Locate the cells, classifying each as a parasitized red blood cell, an uninfected red blood cell, or a white blood cell.
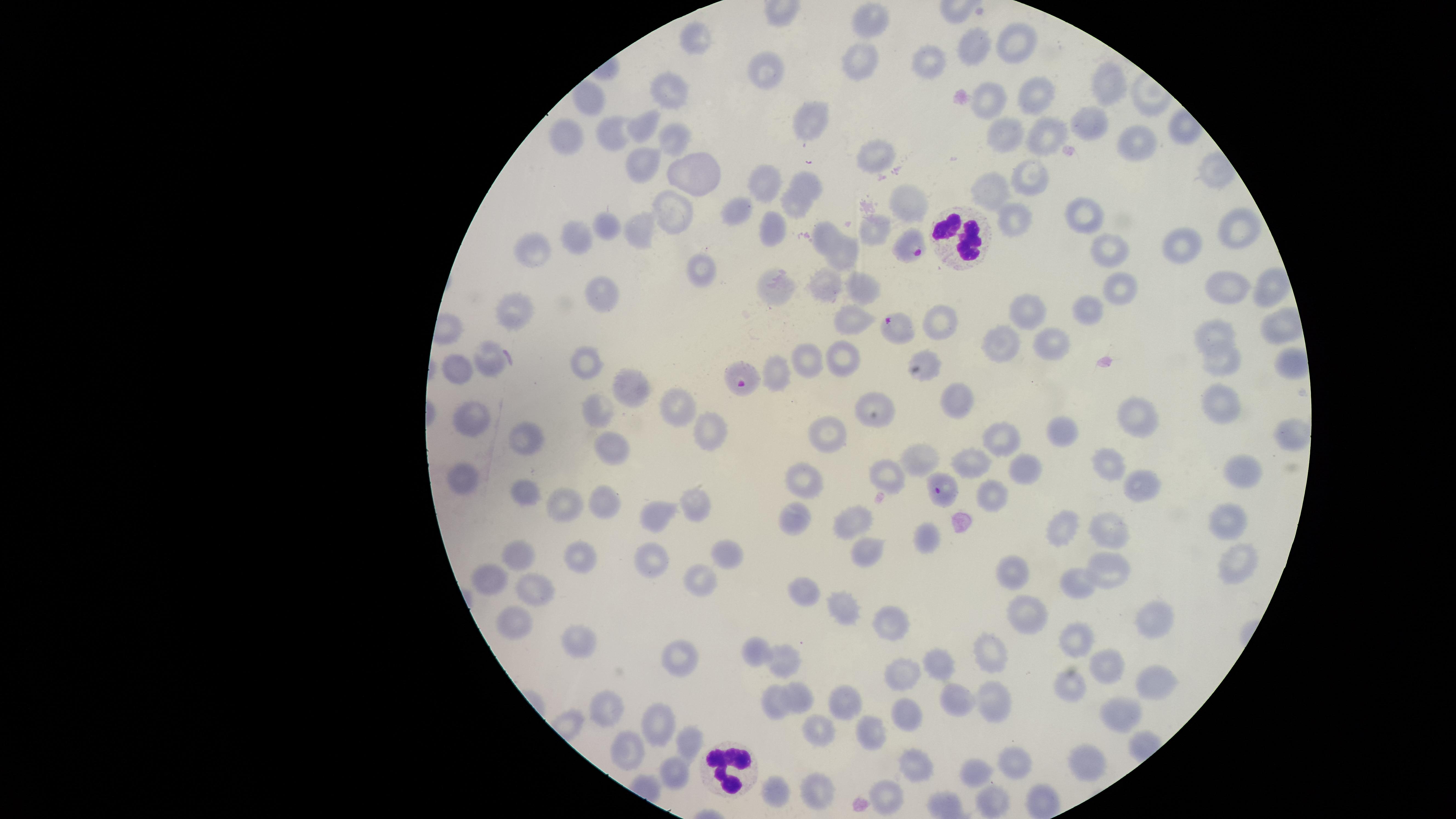
Approximate marker points as {x, y} in pixels.
Parasitized red blood cells: {916, 249}, {895, 330}, {740, 372}, {940, 487}.
Uninfected red blood cells: {871, 20}, {695, 42}, {979, 44}, {1014, 45}, {857, 52}, {926, 57}, {770, 73}, {1104, 88}, {1033, 95}, {671, 97}, {588, 102}, {988, 105}, {813, 124}, {644, 126}, {1089, 126}, {615, 133}, {673, 135}, {1004, 136}, {1043, 136}, {567, 137}, {1142, 143}, {876, 149}, {643, 159}, {692, 175}, {1029, 179}, {773, 180}, {809, 182}, {988, 188}, {910, 193}, {794, 210}, {739, 212}, {1083, 213}, {1013, 218}, {669, 219}, {605, 227}, {637, 229}, {1238, 230}, {772, 232}, {881, 232}, {577, 237}, {825, 239}, {1180, 245}, {529, 247}, {1111, 249}, {844, 253}, {695, 269}, {1229, 285}, {778, 286}, {863, 287}, {1268, 289}, {603, 290}, {825, 290}, {1115, 290}, {1030, 306}, {512, 309}, {1087, 310}, {854, 325}, {934, 326}, {1218, 339}, {1046, 340}, {1003, 344}, {923, 360}, {803, 361}, {1221, 361}, {841, 362}, {488, 363}, {590, 368}, {461, 372}, {774, 375}, {626, 386}, {959, 396}, {673, 402}, {1224, 403}, {875, 410}, {472, 412}, {1138, 413}, {599, 415}, {713, 430}, {1059, 430}, {831, 434}, {1289, 436}, {1007, 437}, {525, 441}, {612, 448}, {915, 460}, {970, 463}, {1111, 464}, {1023, 468}, {1243, 473}, {887, 474}, {461, 480}, {802, 484}, {1141, 487}, {988, 491}, {529, 496}, {697, 500}, {565, 501}, {603, 502}, {659, 514}, {1231, 514}, {794, 515}, {850, 522}, {1064, 525}, {1111, 532}, {922, 535}, {522, 555}, {578, 555}, {722, 555}, {863, 555}, {652, 558}, {1237, 563}, {1105, 565}, {1015, 571}, {490, 576}, {704, 585}, {534, 586}, {1076, 586}, {799, 593}, {843, 608}, {1025, 608}, {1153, 612}, {889, 625}, {509, 626}, {584, 640}, {1077, 641}, {754, 649}, {992, 653}, {678, 657}, {782, 660}, {940, 663}, {1110, 663}, {1157, 680}, {902, 683}, {1066, 686}, {794, 693}, {993, 697}, {843, 704}, {960, 704}, {609, 705}, {774, 705}, {1115, 715}, {662, 719}, {905, 724}, {816, 732}, {868, 733}, {689, 743}, {628, 747}, {1087, 762}, {913, 767}, {1014, 767}, {670, 770}, {973, 772}, {817, 785}, {773, 791}, {887, 800}, {992, 802}.
White blood cells: {961, 234}, {730, 768}.

Summary:
  - Visible region: circular
  - Species: Plasmodium falciparum
  - Capture: smartphone photograph through the microscope eyepiece
  - Image size: 1456×819 pixels
  - Field of view: single
  - Preparation: thin blood film
  - Stain: Giemsa